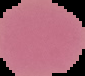
Summary:
  - Image size: 85×76 pixels
  - Result: no Plasmodium parasites seen
  - Preparation: thin blood smear
  - Image type: segmented cell region with the area outside set to black